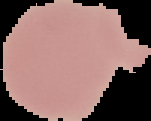

image size = 151×121 pixels
image type = segmented cell region with the area outside set to black
malaria status = uninfected
preparation = thin blood smear